Classify this cell by malaria status.
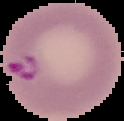

It is parasitized.

From a thin blood film. Cell region segmented out of the field of view; the surrounding area is masked to black. Image is 124×121 pixels.